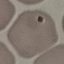
Result: no malaria parasites seen. Thin blood film. Acquired by smartphone through the microscope eyepiece. Giemsa stain. Automatically extracted cell patch, resized to 64 × 64 pixels.